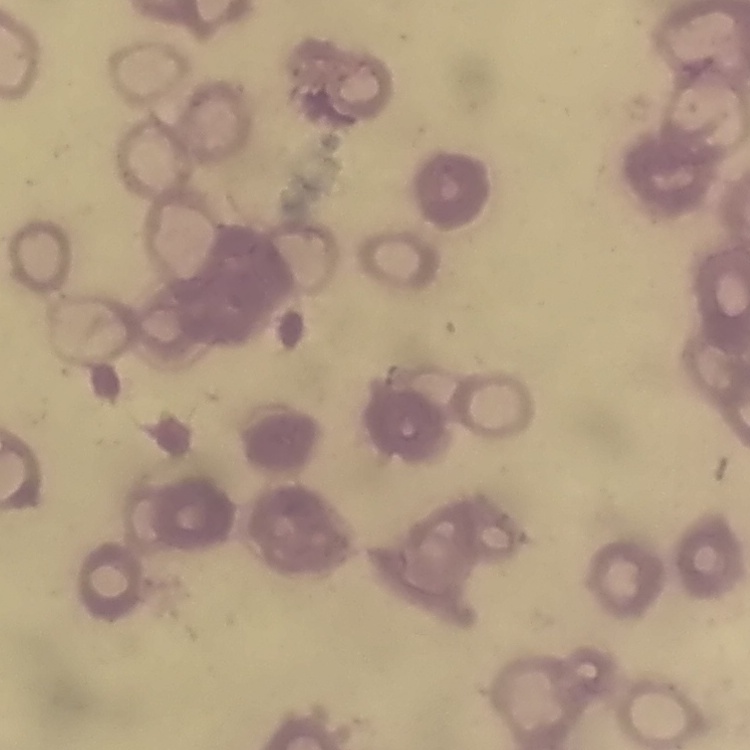
Summary:
  - Erythrocyte morphology: rouleaux formation
  - Stain: Field's or Giemsa
  - Preparation: thin blood film
  - Image type: square crop of a larger photomicrograph